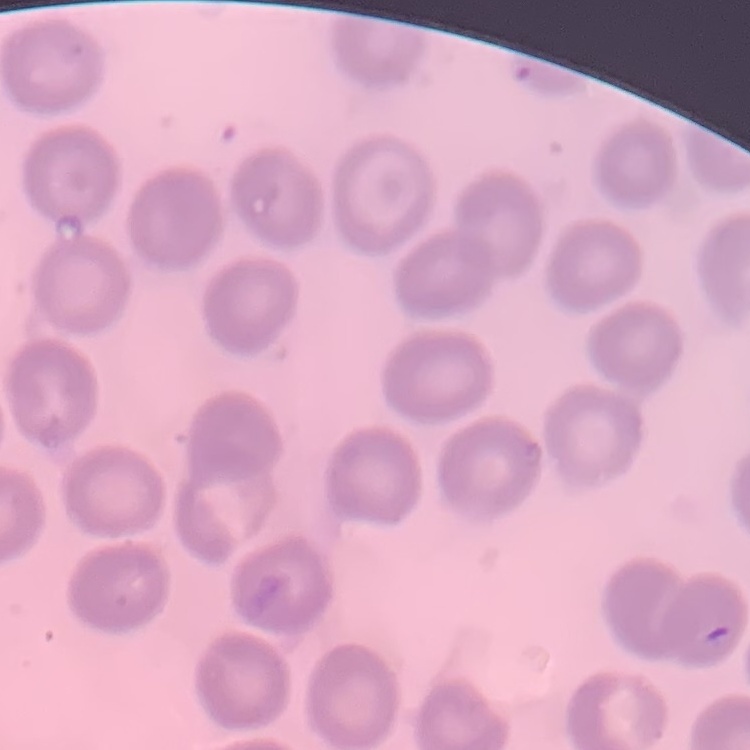
Summary:
  - Red blood cell morphology: no rouleaux formation
  - Stain: Field's or Giemsa
  - Preparation: thin blood film
  - Image type: square crop of a larger photomicrograph